Name the parasite shown.
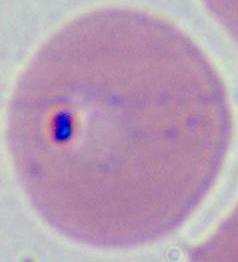

This is Plasmodium.

magnification = 400x or 1000x
modality = micrograph